State which parasite is depicted.
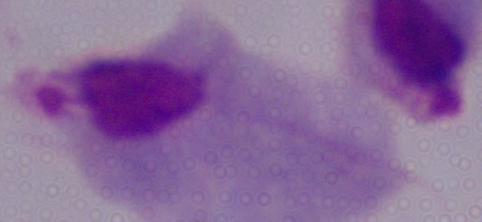
A trichomonad.

Summary:
  - Modality: photomicrograph
  - Magnification: 1000x